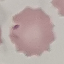

Summary:
  - Result: no malaria parasites detected
  - Image type: cell patch, automatically extracted from a larger field of view and resized to 64 × 64 pixels
  - Stain: Giemsa
  - Capture: smartphone through the microscope eyepiece
  - Preparation: thin blood film